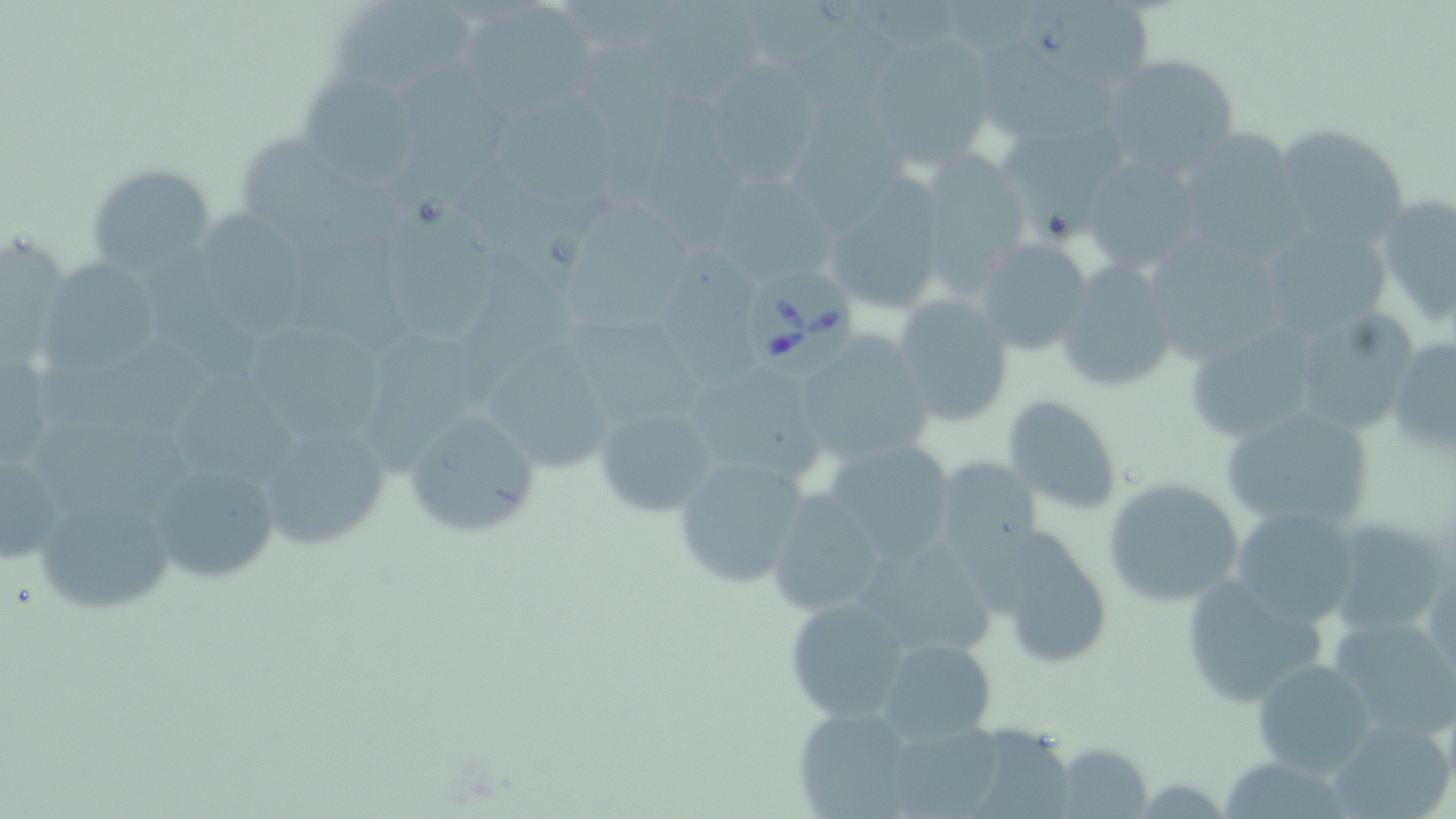
{
  "babesia_divergens_infected_red_blood_cell_locations": "approximate bounding boxes as (x1,y1)-(x2,y2) corner pairs in pixels: (747,272)-(865,379)",
  "slide_level_diagnosis": "Babesia divergens",
  "field_of_view": "one of a larger specimen",
  "magnification": "1000x",
  "image_size": "1456×819 pixels",
  "uninfected_red_blood_cell_locations": "approximate bounding boxes as (x1,y1)-(x2,y2) corner pairs in pixels: (332,0)-(473,98), (1022,0)-(1166,85), (651,1)-(772,103), (453,2)-(600,115), (790,14)-(902,114), (877,34)-(997,179), (980,38)-(1134,150), (581,39)-(686,213), (1100,53)-(1241,180), (709,58)-(812,190), (386,60)-(518,214), (299,71)-(421,188), (490,88)-(631,210), (781,96)-(925,245), (998,120)-(1136,255), (1270,124)-(1413,251), (1168,128)-(1310,259), (233,136)-(401,266), (915,151)-(1032,287), (1079,154)-(1205,276), (456,163)-(609,287), (87,164)-(217,273), (719,177)-(833,293), (818,178)-(950,316), (383,194)-(497,341), (1372,194)-(1456,328), (553,202)-(700,338), (205,208)-(311,344), (1241,219)-(1398,345), (294,229)-(414,355), (1141,234)-(1291,368), (974,238)-(1094,357), (137,239)-(269,382), (659,243)-(765,399), (456,252)-(577,409), (36,253)-(169,377), (1055,260)-(1179,394), (891,294)-(1015,427), (1284,305)-(1421,440), (567,318)-(707,430), (244,320)-(391,447), (1183,322)-(1322,447), (366,327)-(480,484), (480,333)-(614,481), (792,333)-(933,465), (1386,336)-(1456,457), (32,348)-(214,439), (683,364)-(825,487), (177,373)-(303,490), (1002,395)-(1123,517), (592,401)-(720,519), (1218,402)-(1376,535), (399,407)-(542,541), (29,414)-(201,521), (268,434)-(391,557), (822,434)-(957,562), (0,445)-(72,570), (671,453)-(813,591), (933,456)-(1041,561), (146,459)-(282,589), (1102,477)-(1246,608), (28,487)-(176,615), (765,490)-(889,618), (1231,505)-(1362,626), (1324,517)-(1454,642), (979,526)-(1117,668), (851,532)-(1001,668), (1423,557)-(1455,686), (1179,576)-(1328,708), (783,596)-(912,723), (1328,615)-(1456,743), (877,637)-(997,744), (1251,658)-(1377,779), (792,706)-(915,817), (1327,716)-(1455,819), (888,721)-(1015,819), (970,729)-(1088,817), (1054,742)-(1151,817)",
  "modality": "optical microscopy",
  "stain": "May-Grünwald-Giemsa",
  "preparation": "thin blood film"
}